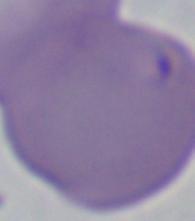
{
  "modality": "photomicrograph",
  "identification": "Babesia",
  "magnification": "1000x"
}